Give the position of every Plasmodium parasite.
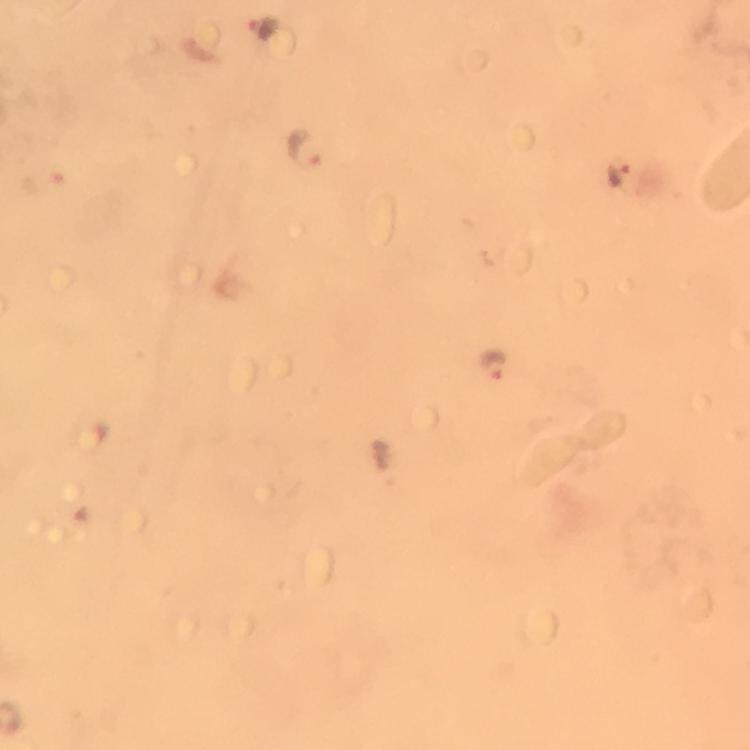

Approximate centers as [x, y] in pixels.
Plasmodium parasites: [261, 27], [308, 148], [621, 171], [495, 367].

Cropped region of a single field of view. Immersion oil was used. Thick blood smear. Smartphone photograph taken through a microscope. Image is 750×750 pixels. From a diagnostic examination for malaria. Giemsa stain. 100x magnification.